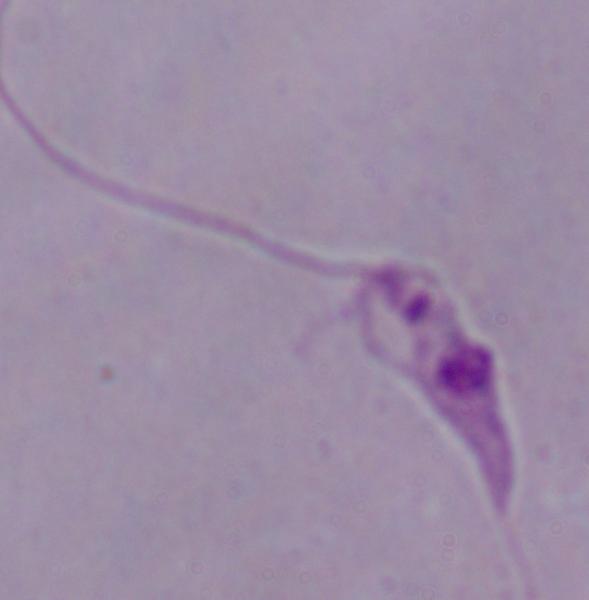
magnification = 1000x
modality = photomicrograph
identification = Leishmania